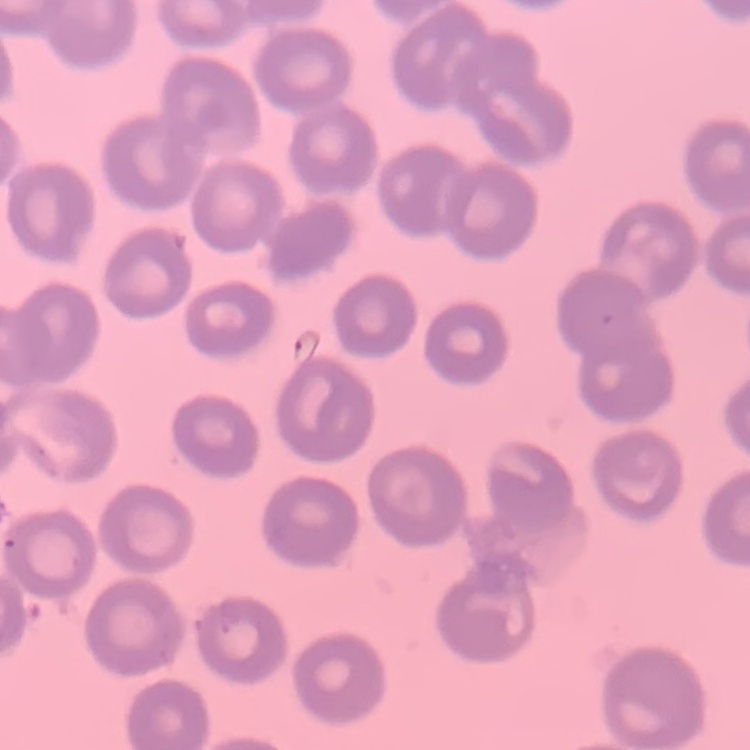
The red blood cells show no rouleaux formation. One tile cut from a larger photomicrograph. Thin blood smear. Field's or Giemsa stain.